Locate every blood parasite and identify its species.
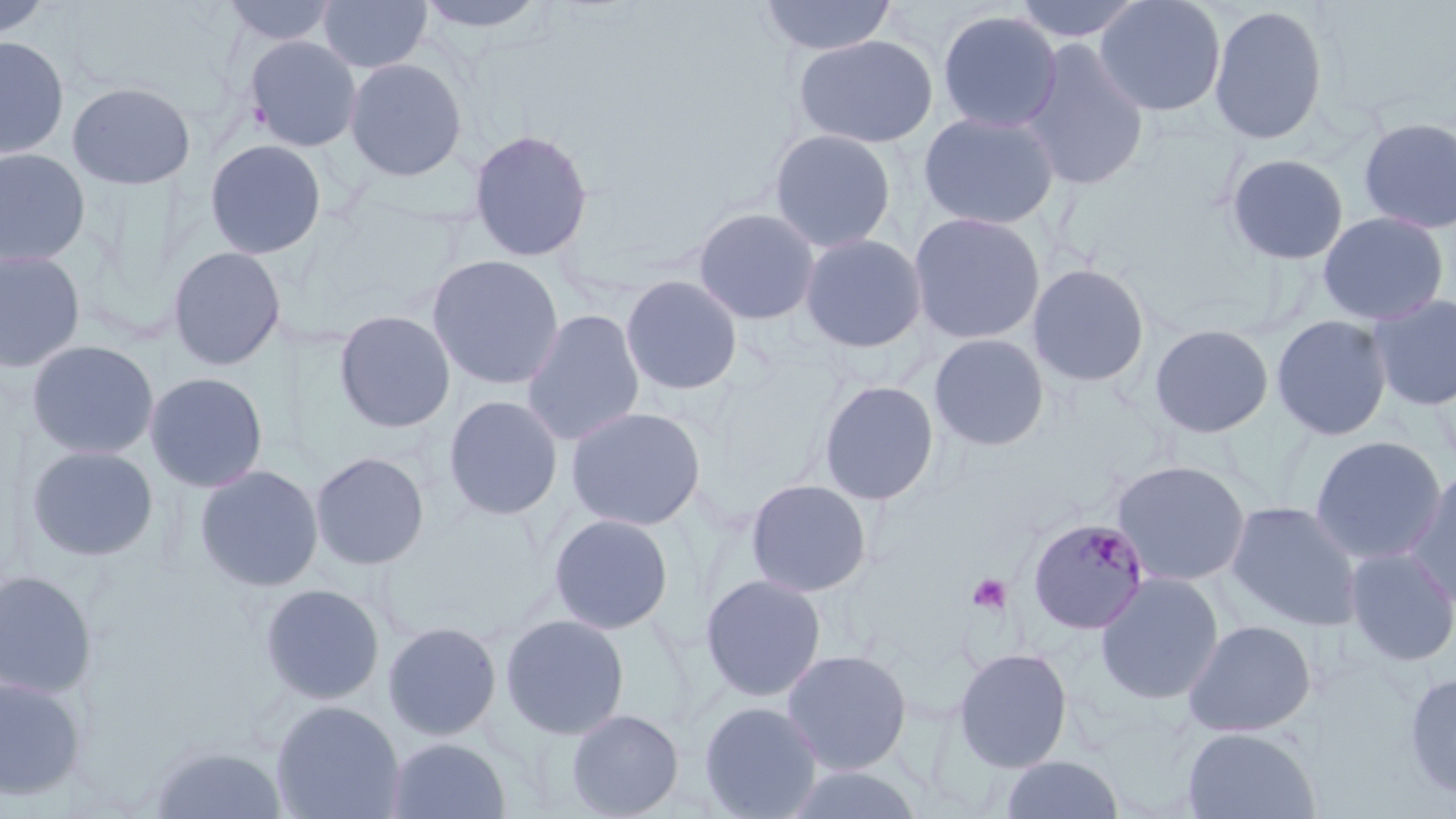
Approximate bounding boxes as (x1, y1, x2, y2) in pixels.
Plasmodium malariae-infected red blood cells: (1027, 517, 1150, 635).
No Plasmodium falciparum, Plasmodium ovale, Plasmodium vivax, Babesia divergens, or Trypanosoma brucei observed.

Summary:
  - Uninfected red blood cell locations: (220, 0, 340, 47), (318, 0, 432, 73), (416, 0, 551, 35), (758, 0, 898, 57), (1008, 0, 1149, 44), (1093, 0, 1228, 117), (0, 1, 53, 41), (1208, 4, 1328, 146), (936, 9, 1062, 134), (793, 33, 939, 149), (0, 35, 70, 159), (243, 36, 362, 153), (1020, 39, 1150, 191), (344, 57, 468, 181), (67, 81, 196, 190), (917, 110, 1061, 230), (1357, 117, 1456, 234), (468, 128, 594, 263), (768, 128, 897, 253), (204, 138, 328, 260), (0, 148, 92, 268), (1224, 153, 1349, 266), (693, 207, 821, 325), (1317, 211, 1449, 326), (908, 212, 1045, 345), (799, 233, 927, 353), (166, 245, 286, 371), (0, 249, 86, 373), (425, 254, 565, 391), (1027, 263, 1151, 388), (620, 274, 743, 396), (1368, 293, 1456, 411), (521, 308, 646, 446), (334, 309, 456, 434), (1270, 314, 1394, 441), (1148, 323, 1275, 438), (928, 333, 1051, 451), (25, 340, 159, 461), (144, 371, 269, 493), (817, 380, 940, 505), (443, 394, 565, 521), (565, 406, 706, 531), (1309, 435, 1447, 564), (25, 444, 160, 563), (310, 451, 430, 571), (1112, 460, 1251, 586), (193, 464, 324, 592), (1404, 467, 1456, 609), (745, 478, 872, 597), (1225, 500, 1363, 630), (547, 513, 674, 635), (1343, 547, 1456, 666), (0, 569, 98, 699), (1095, 572, 1224, 705), (700, 574, 826, 702), (258, 583, 386, 705), (499, 613, 630, 739), (1183, 619, 1316, 737), (381, 621, 503, 741), (952, 647, 1073, 773), (782, 649, 912, 774), (1403, 670, 1456, 801), (0, 672, 88, 802), (270, 700, 405, 819), (698, 701, 823, 818), (565, 708, 684, 818), (1181, 726, 1321, 819), (384, 736, 512, 819), (147, 741, 290, 819), (1000, 755, 1124, 818), (777, 764, 928, 819)
  - Platelet locations: (967, 573, 1013, 615)
  - Slide-level diagnosis: Plasmodium malariae
  - Magnification: 1000x
  - Stain: May-Grünwald-Giemsa
  - Preparation: thin blood smear
  - Image size: 1456×819 pixels
  - Field of view: single
  - Modality: light microscopy